Give the position of every malaria parasite.
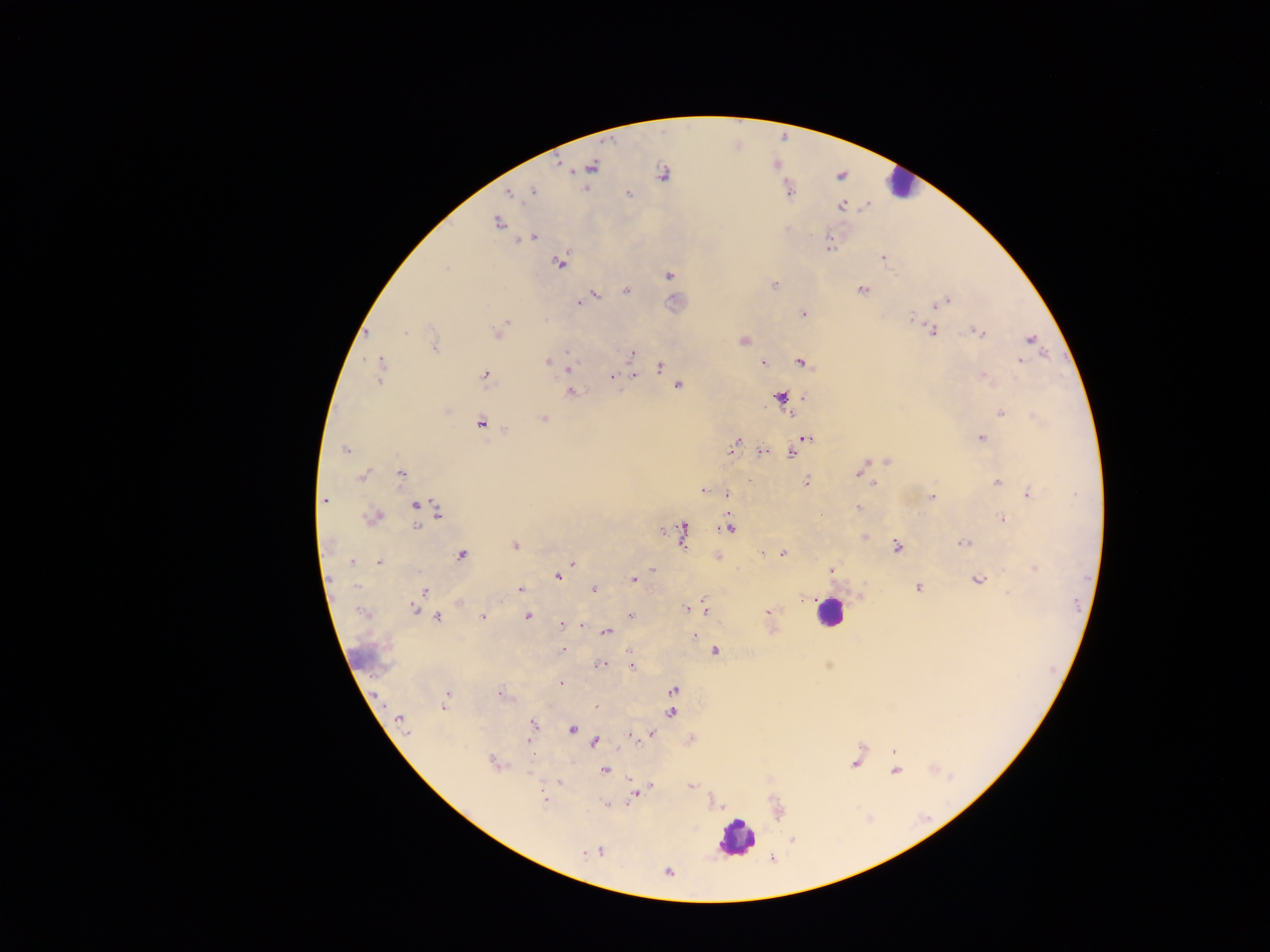

Approximate centers as x y in pixels.
Malaria parasites: 561 165; 592 167; 663 173; 533 192; 628 193; 508 194; 842 205; 496 223; 532 238; 829 244; 882 256; 559 263; 446 268; 669 275; 775 285; 861 290; 625 291; 593 295; 578 302; 944 302; 939 305; 803 314; 912 317; 504 322; 932 330; 980 332; 405 333; 498 334; 1029 339; 743 341; 434 348; 567 353; 631 354; 1020 360; 547 361; 381 362; 764 363; 801 363; 661 367; 568 368; 380 370; 485 375; 634 375; 983 375; 612 376; 380 380; 678 385; 569 392; 781 398; 805 398; 1001 414; 543 418; 481 423; 981 437; 805 438; 734 446; 344 449; 763 452; 791 453; 887 461; 865 462; 401 473; 858 473; 361 476; 806 482; 873 483; 996 483; 703 491; 1030 493; 727 495; 932 497; 325 501; 416 504; 858 508; 438 513; 376 516; 1003 519; 417 527; 729 527; 661 530; 682 532; 864 537; 964 544; 515 546; 897 546; 762 553; 782 554; 461 556; 352 562; 573 562; 379 563; 653 569; 1035 569; 831 570; 558 577; 978 579; 633 580; 918 588; 520 589; 594 589; 425 591; 1008 593; 414 609; 687 609; 705 609; 360 611; 768 612; 630 616; 483 617; 528 617; 437 618; 562 625; 582 626; 605 632; 694 636; 563 650; 630 652; 715 652; 601 665; 631 667; 561 683; 673 690; 501 694; 447 695; 597 706; 444 708; 671 712; 399 720; 533 724; 572 729; 407 732; 651 734; 631 735; 528 740; 595 743; 893 751; 533 755; 494 763; 855 763; 604 770; 895 771; 630 780; 559 782; 651 786; 691 786; 634 796; 543 798; 606 805; 599 852; 586 853; 668 873.

Leukocyte locations: 898 182; 829 612; 737 837. One field of view. Image is 1270×952 pixels. Collected in Ghana. Thick blood film. Mobile-phone photograph taken through the microscope.